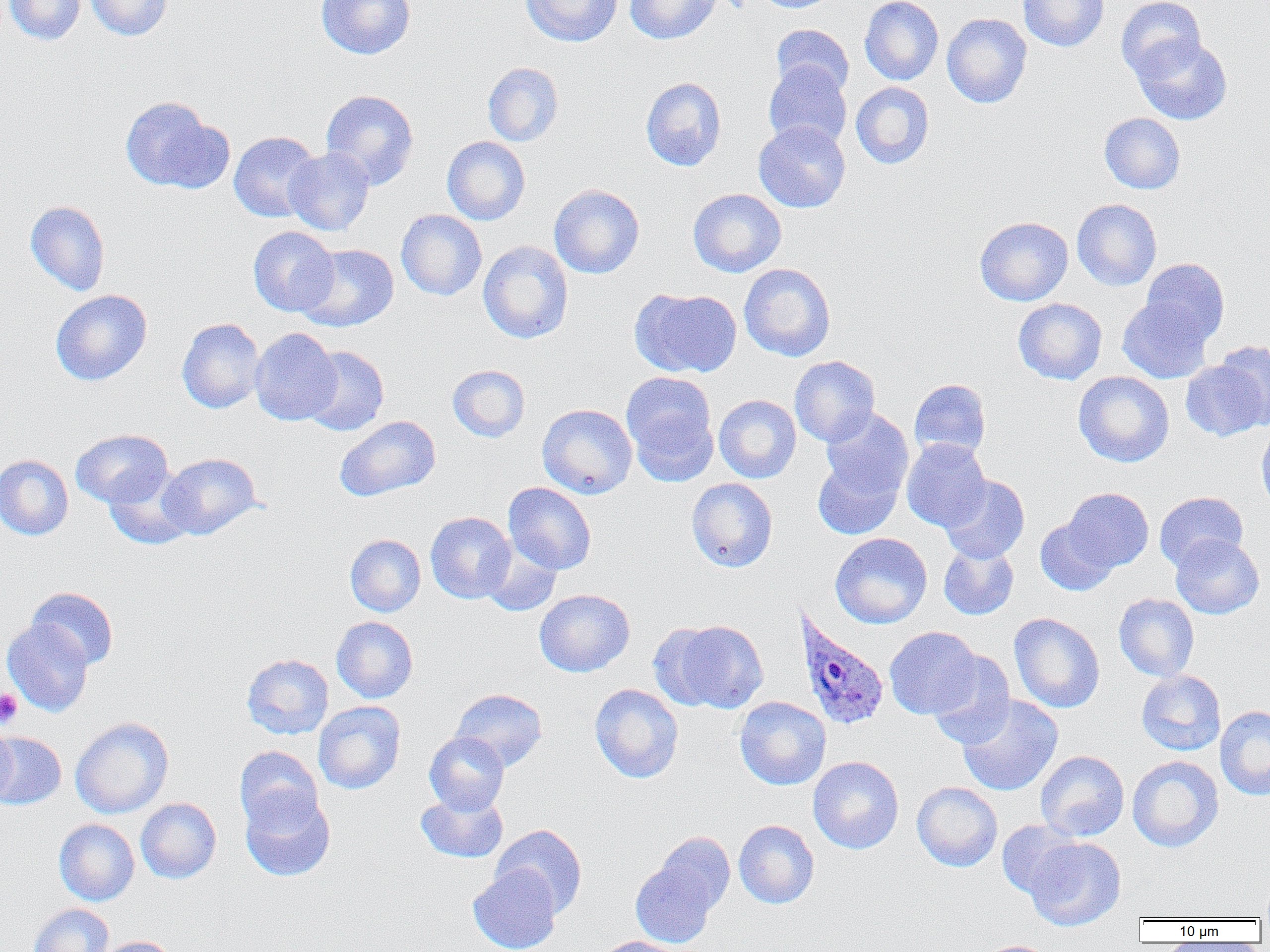 Approximate bounding boxes as [x1, y1, x2, y2] in pixels. Platelet locations: [0, 689, 22, 729]. Uninfected red blood cell locations: [3, 0, 85, 45], [85, 0, 172, 41], [316, 0, 416, 59], [521, 0, 622, 47], [625, 0, 721, 45], [755, 0, 840, 13], [860, 0, 944, 85], [1018, 0, 1109, 52], [1115, 0, 1206, 81], [942, 13, 1032, 108], [772, 24, 854, 96], [1131, 35, 1232, 125], [763, 61, 852, 150], [483, 62, 564, 146], [641, 77, 727, 171], [850, 82, 934, 169], [320, 89, 419, 189], [120, 96, 230, 194], [1099, 113, 1185, 194], [753, 120, 850, 213], [229, 131, 322, 222], [442, 136, 530, 225], [284, 147, 375, 236], [549, 184, 645, 278], [688, 188, 786, 277], [1072, 199, 1162, 291], [25, 200, 110, 296], [396, 209, 487, 301], [975, 216, 1073, 306], [248, 226, 339, 316], [478, 240, 574, 344], [296, 243, 399, 332], [1141, 258, 1230, 345], [739, 263, 835, 362], [631, 287, 741, 378], [50, 290, 152, 386], [1118, 296, 1212, 384], [1013, 298, 1107, 384], [177, 317, 265, 413], [249, 328, 342, 426], [1215, 340, 1270, 431], [301, 346, 389, 436], [789, 356, 880, 446], [1180, 360, 1266, 441], [447, 364, 530, 442], [621, 371, 718, 481], [1073, 371, 1174, 467], [909, 379, 991, 460], [714, 394, 801, 483], [537, 403, 637, 499], [820, 407, 914, 502], [335, 415, 441, 502], [1256, 423, 1270, 515], [71, 429, 173, 508], [901, 439, 990, 531], [158, 452, 261, 540], [0, 454, 73, 540], [812, 454, 905, 539], [104, 468, 194, 550], [939, 475, 1030, 563], [686, 478, 778, 572], [503, 482, 596, 574], [1061, 487, 1154, 574], [1154, 492, 1248, 571], [425, 511, 516, 603], [1035, 515, 1120, 596], [830, 533, 932, 628], [1170, 533, 1264, 619], [345, 534, 426, 617], [480, 537, 562, 616], [938, 542, 1019, 620], [27, 587, 119, 670], [534, 589, 635, 677], [1114, 593, 1199, 681], [1009, 612, 1105, 713], [331, 616, 418, 703], [660, 619, 769, 713], [2, 620, 94, 717], [884, 626, 981, 719], [927, 651, 1015, 748], [241, 653, 333, 739], [1136, 670, 1226, 756], [589, 683, 684, 783], [450, 688, 548, 771], [956, 694, 1063, 796], [734, 696, 831, 790], [313, 701, 405, 794], [1216, 705, 1270, 800], [70, 716, 174, 818], [0, 724, 18, 808], [424, 731, 509, 815], [0, 733, 67, 810], [234, 746, 323, 830], [1036, 750, 1129, 841], [1127, 755, 1223, 852], [808, 756, 904, 854], [912, 781, 1003, 871], [240, 787, 335, 881], [416, 790, 508, 863], [135, 797, 221, 884], [54, 819, 140, 906], [733, 819, 819, 909], [996, 820, 1085, 901], [491, 824, 587, 918], [653, 831, 735, 915], [1024, 836, 1126, 931], [630, 858, 721, 948], [468, 864, 561, 952], [28, 904, 113, 952], [96, 936, 179, 952], [595, 937, 689, 952], [975, 940, 1058, 952]. Plasmodium ovale-infected red blood cell locations: [793, 608, 890, 731]. Slide-level diagnosis: Plasmodium ovale. Captured at 1000x magnification. Thin blood smear. One field of a larger specimen. Image is 1270×952 pixels. Optical microscopy.